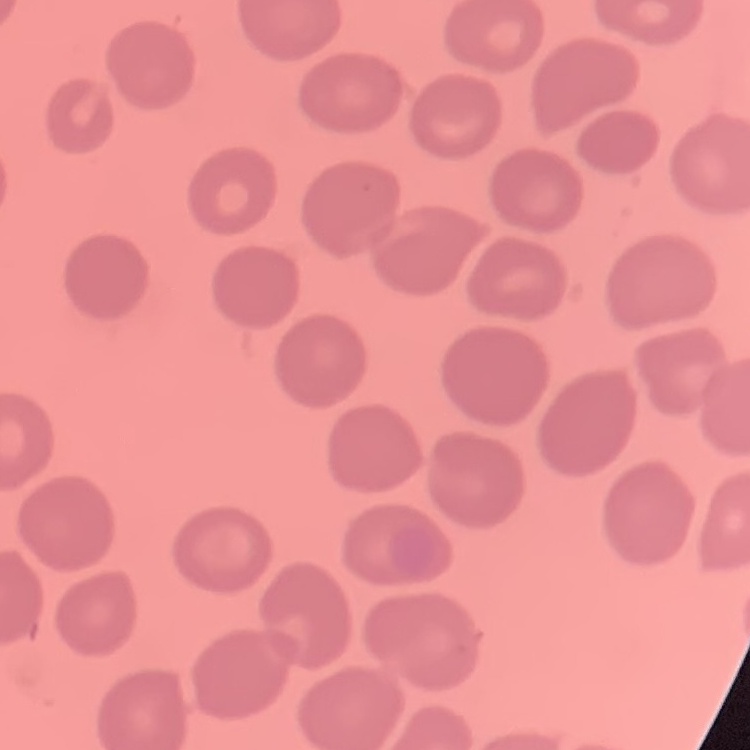
The red blood cells show no rouleaux formation. Stained with either Field's or Giemsa. One tile cut from a larger photomicrograph. Thin peripheral smear.